Give the position of every malaria parasite.
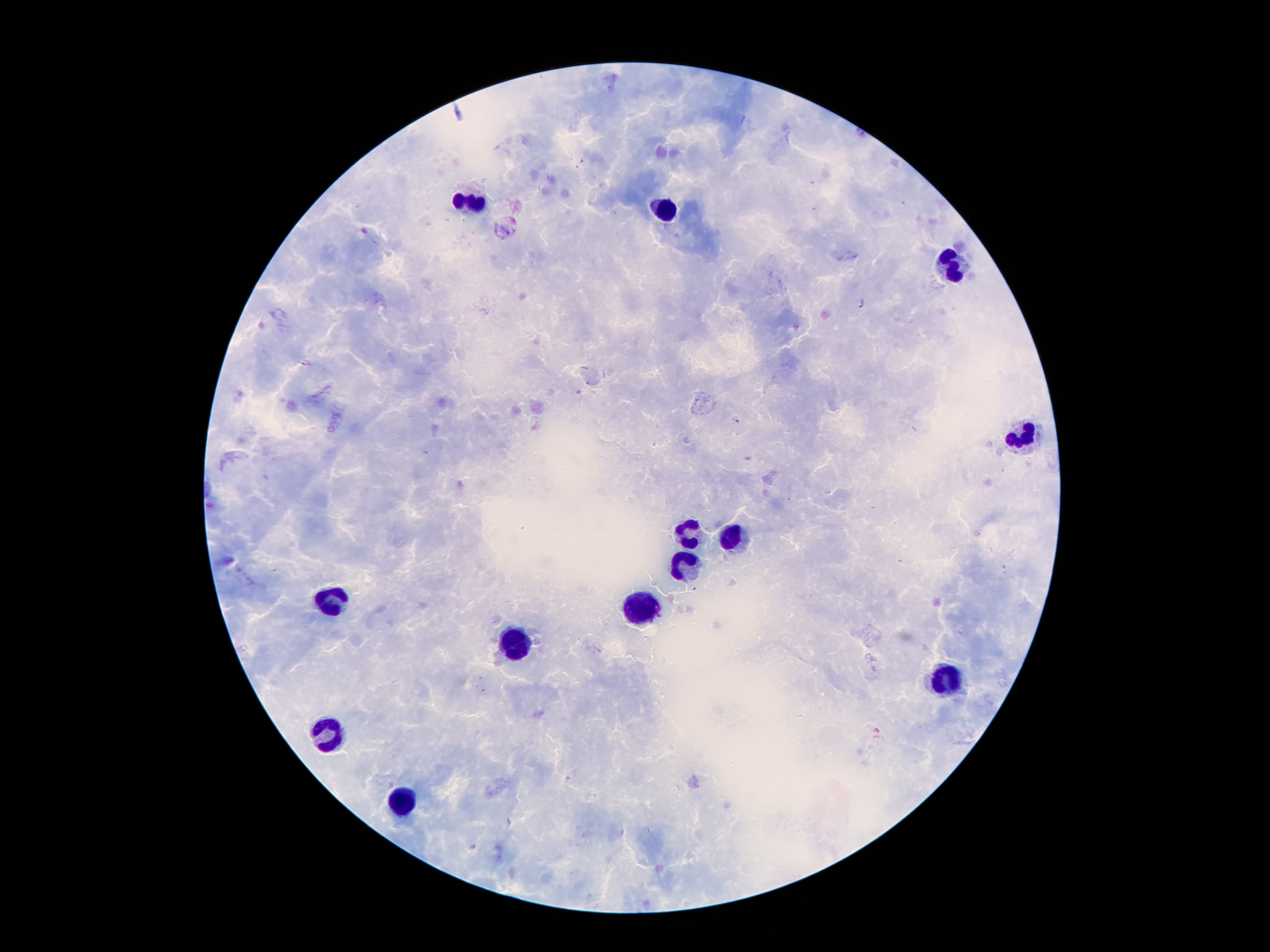

Approximate centers as [x, y] in pixels.
Malaria parasites: [862, 303], [307, 363], [736, 418].

Summary:
  - Leukocyte locations: [471, 201], [665, 211], [950, 269], [1024, 438], [690, 533], [731, 538], [688, 565], [336, 599], [647, 604], [516, 642], [949, 679], [329, 733], [402, 799]
  - Capture: smartphone camera through the microscope eyepiece
  - Magnification: 100x
  - Image size: 1270×952 pixels
  - Field of view: single
  - Patient malaria status: positive for Plasmodium falciparum
  - Preparation: thick peripheral-blood smear
  - Stain: Giemsa